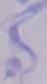 Photomicrograph. Captured at 1000x magnification. A trypanosome is shown.